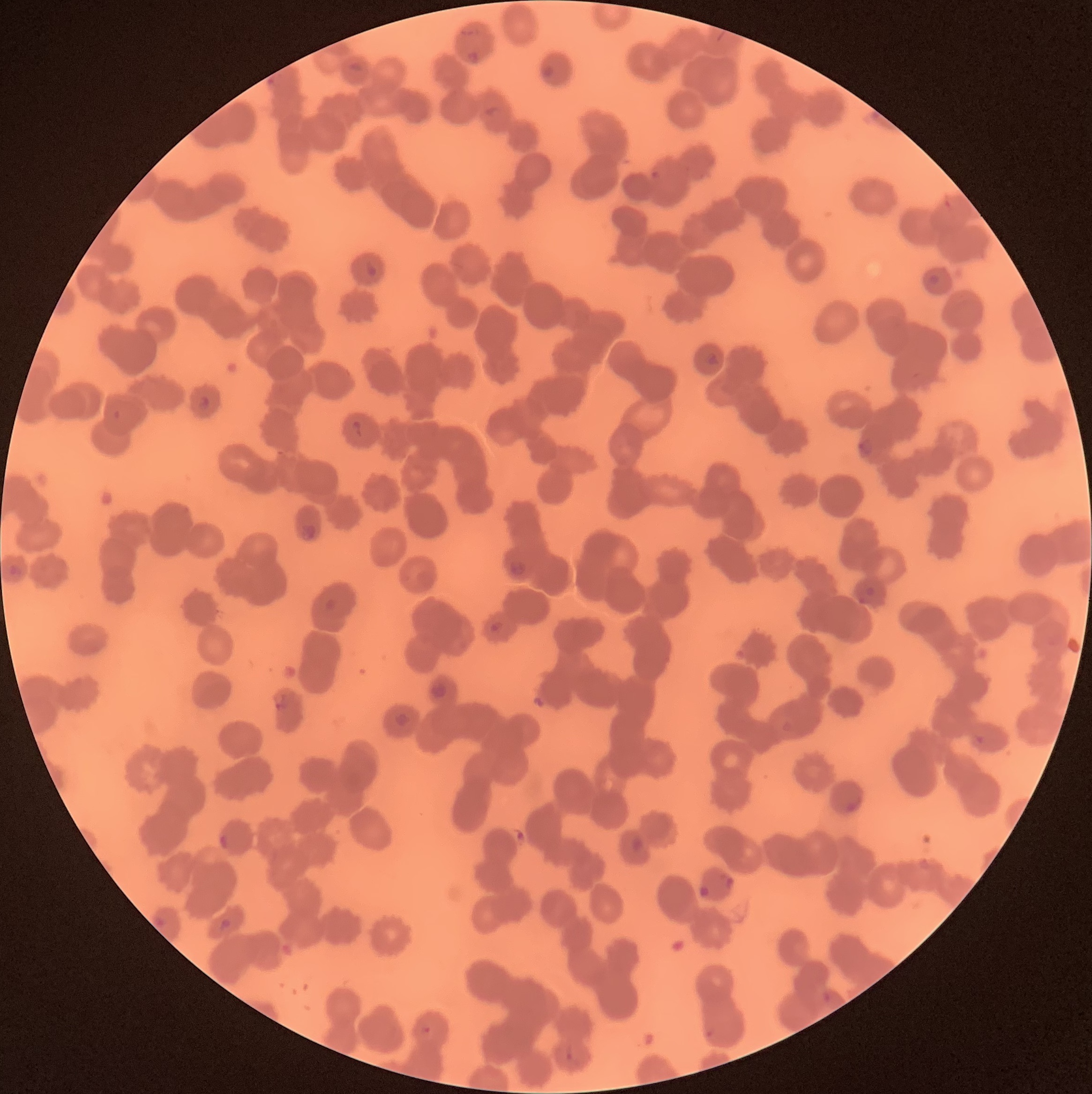 Approximate bounding boxes as [x1, y1, x2, y2] in pixels. Plasmodium parasite locations: [469, 50, 479, 62], [351, 62, 365, 74], [543, 65, 553, 79], [267, 78, 277, 86], [486, 105, 501, 116], [651, 170, 664, 181], [366, 259, 378, 278], [200, 393, 211, 410], [353, 419, 364, 436], [858, 439, 872, 458], [302, 522, 315, 540], [505, 559, 530, 584], [867, 586, 875, 595], [488, 622, 504, 636], [274, 696, 288, 712], [782, 721, 792, 733], [975, 733, 985, 745], [847, 798, 862, 810], [219, 835, 229, 852], [919, 856, 931, 869], [720, 870, 735, 891], [155, 917, 168, 929], [219, 918, 231, 930], [823, 991, 830, 1005], [420, 1024, 432, 1040], [706, 1029, 713, 1040], [565, 1045, 573, 1062]. Plasmodium parasites too small for a box (approximate centers as [x, y] in pixels): [863, 601]. Thin blood film. Image is 1092×1094 pixels. Optical microscopy. The red blood cells show rouleaux formation.